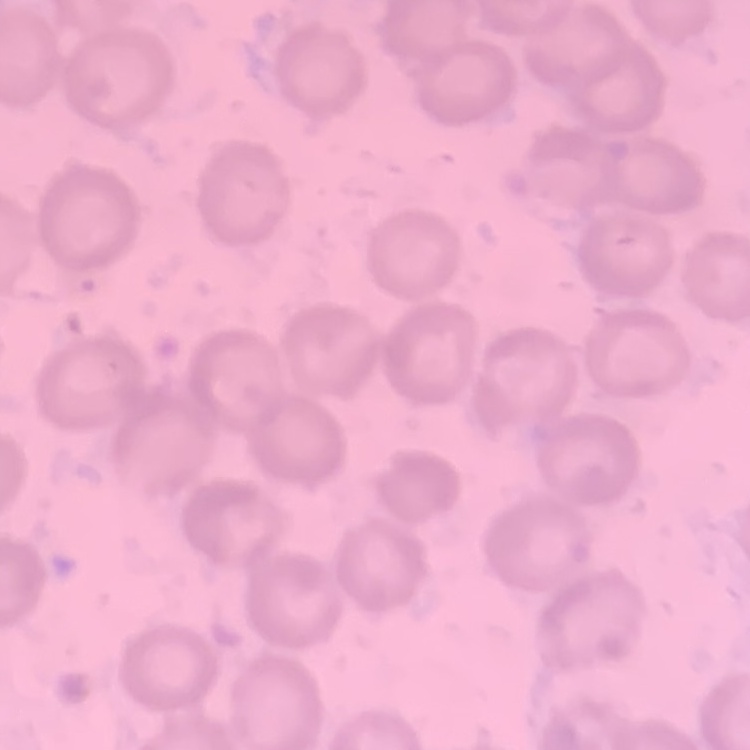

The erythrocytes show no rouleaux formation. One tile cut from a larger photomicrograph. Stained with either Field's or Giemsa. Thin blood smear.